Assess this cell for malaria.
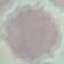

It is uninfected.

Summary:
  - Capture: smartphone through the microscope eyepiece
  - Preparation: thin blood smear
  - Image type: cell patch, automatically extracted from a larger field of view and resized to 64 × 64 pixels
  - Stain: Giemsa